Locate and identify every blood parasite.
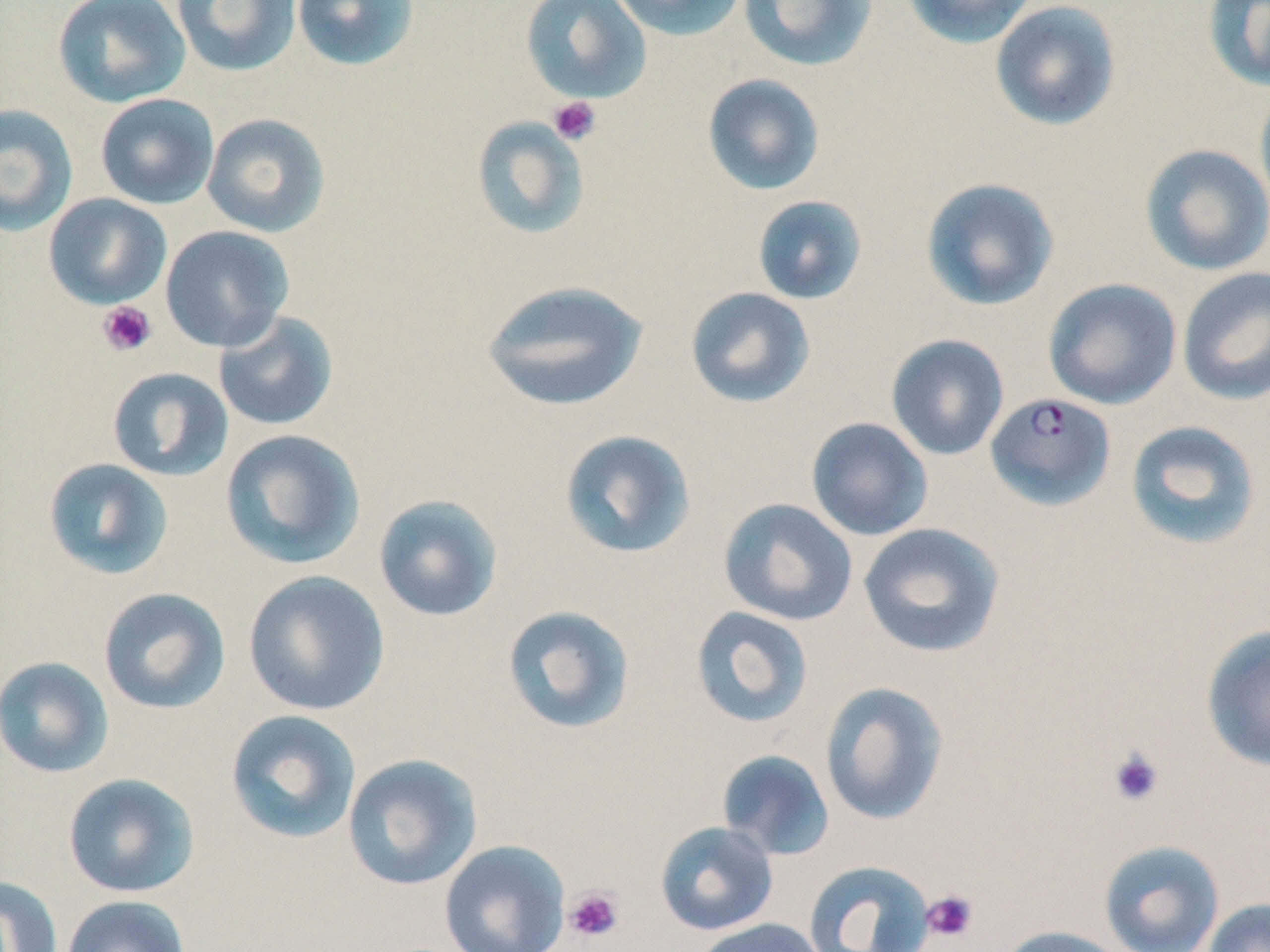
Approximate bounding boxes as (x1,y1)-(x2,y2) corner pairs in pixels.
Plasmodium falciparum-infected red blood cells: (985,392)-(1115,510).
No Plasmodium ovale, Plasmodium malariae, Plasmodium vivax, Babesia divergens, or Trypanosoma brucei observed.

Platelet locations: (548,96)-(601,146), (97,301)-(157,356), (1107,747)-(1165,807), (564,887)-(624,943), (921,889)-(978,943). Uninfected red blood cell locations: (52,0)-(191,108), (170,0)-(303,77), (291,0)-(421,73), (520,0)-(652,104), (609,0)-(747,42), (738,0)-(879,72), (901,0)-(1039,49), (1202,0)-(1270,93), (989,1)-(1122,131), (702,73)-(826,196), (1254,82)-(1270,218), (95,93)-(219,209), (0,103)-(79,237), (201,113)-(331,238), (471,115)-(592,240), (1139,144)-(1270,277), (920,177)-(1060,312), (43,193)-(173,310), (752,195)-(867,305), (159,225)-(294,352), (1176,267)-(1270,406), (1043,278)-(1181,410), (481,279)-(650,412), (685,287)-(816,409), (213,311)-(339,431), (886,334)-(1009,460), (107,367)-(233,482), (805,417)-(933,541), (1125,420)-(1263,551), (220,428)-(366,570), (559,429)-(697,559), (43,457)-(174,581), (373,494)-(504,622), (718,498)-(858,626), (857,523)-(1005,658), (242,569)-(390,716), (98,587)-(231,715), (501,604)-(636,735), (690,606)-(815,729), (1201,624)-(1270,772), (0,656)-(114,778), (819,682)-(949,826), (224,709)-(362,844), (715,749)-(835,861), (342,752)-(483,890), (62,773)-(200,898), (654,821)-(778,936), (439,839)-(570,952), (1099,840)-(1225,952), (803,860)-(935,952), (0,875)-(63,952), (61,894)-(191,952), (1203,899)-(1270,952), (691,917)-(827,952), (998,925)-(1131,952). Slide-level diagnosis: Plasmodium falciparum. One field of a larger specimen. Image is 1270×952 pixels. Thin blood film. Optical microscopy. 1000x magnification. May-Grünwald-Giemsa-stained preparation.